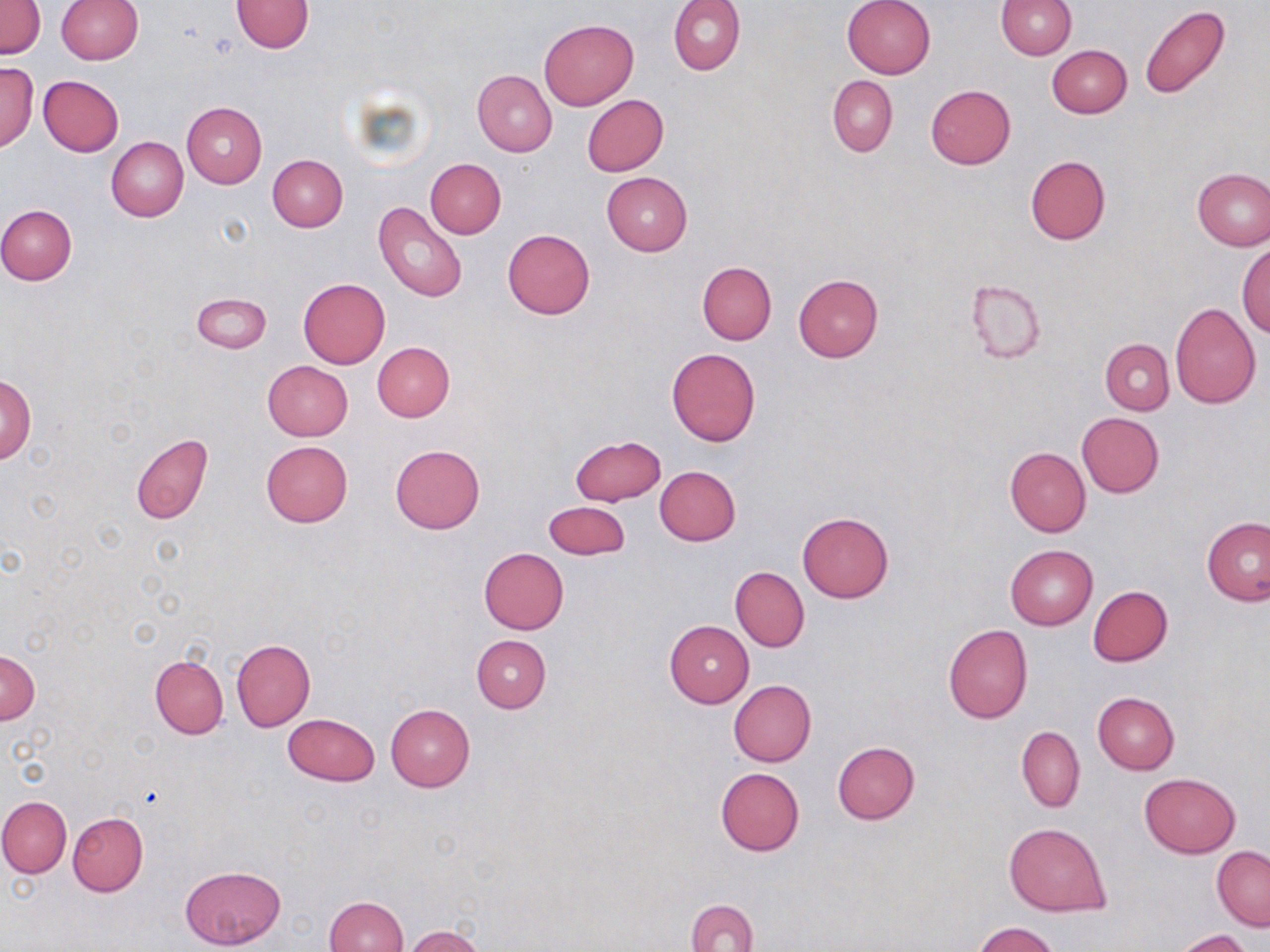

slide-level diagnosis = no evidence of blood parasites
uninfected red blood cell locations = approximate bounding boxes as (x1, y1, x2, y2) in pixels: (0, 0, 45, 59), (230, 0, 314, 52), (670, 0, 746, 75), (842, 0, 936, 78), (995, 0, 1076, 59), (56, 1, 142, 65), (1140, 5, 1232, 99), (539, 19, 638, 109), (1047, 46, 1131, 118), (0, 62, 38, 151), (472, 69, 557, 157), (38, 75, 124, 156), (828, 75, 897, 157), (926, 84, 1016, 169), (582, 94, 669, 176), (181, 101, 267, 188), (106, 137, 188, 221), (267, 155, 347, 232), (1024, 155, 1111, 246), (425, 158, 506, 239), (1192, 168, 1270, 251), (602, 172, 692, 256), (373, 200, 467, 302), (0, 205, 76, 285), (502, 228, 596, 319), (1237, 244, 1270, 336), (697, 261, 776, 345), (793, 274, 883, 361), (298, 278, 391, 367), (964, 278, 1046, 365), (192, 293, 271, 352), (1169, 302, 1262, 408), (1100, 339, 1174, 414), (372, 342, 454, 421), (667, 347, 761, 447), (262, 360, 352, 440), (2, 375, 36, 464), (1076, 412, 1164, 498), (131, 434, 213, 523), (569, 435, 667, 506), (260, 441, 352, 528), (390, 445, 487, 534), (1004, 447, 1091, 536), (655, 465, 741, 546), (542, 502, 630, 560), (797, 510, 893, 603), (1202, 517, 1270, 606), (1005, 544, 1098, 630), (479, 547, 569, 634), (731, 566, 809, 651), (1087, 586, 1173, 666), (665, 621, 754, 707), (943, 624, 1033, 723), (471, 635, 552, 712), (231, 638, 315, 731), (1, 652, 40, 724), (149, 655, 227, 739), (728, 680, 816, 766), (1092, 692, 1180, 775), (385, 703, 475, 791), (283, 712, 381, 786), (1017, 725, 1085, 813), (831, 742, 920, 824), (716, 768, 804, 855), (1139, 773, 1241, 858), (0, 795, 71, 877), (68, 811, 148, 896), (1003, 823, 1112, 916), (1211, 846, 1269, 930), (179, 865, 286, 950), (325, 895, 407, 952), (687, 898, 757, 952), (973, 922, 1061, 952), (400, 925, 488, 952), (1174, 930, 1251, 952)
field of view = one of a larger specimen
stain = May-Grünwald-Giemsa
image size = 1270×952 pixels
modality = optical microscopy
magnification = 1000x
preparation = thin blood film